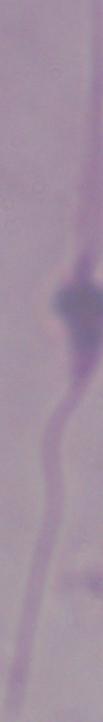 Photomicrograph. Captured at 1000x magnification. A Leishmania parasite is shown.